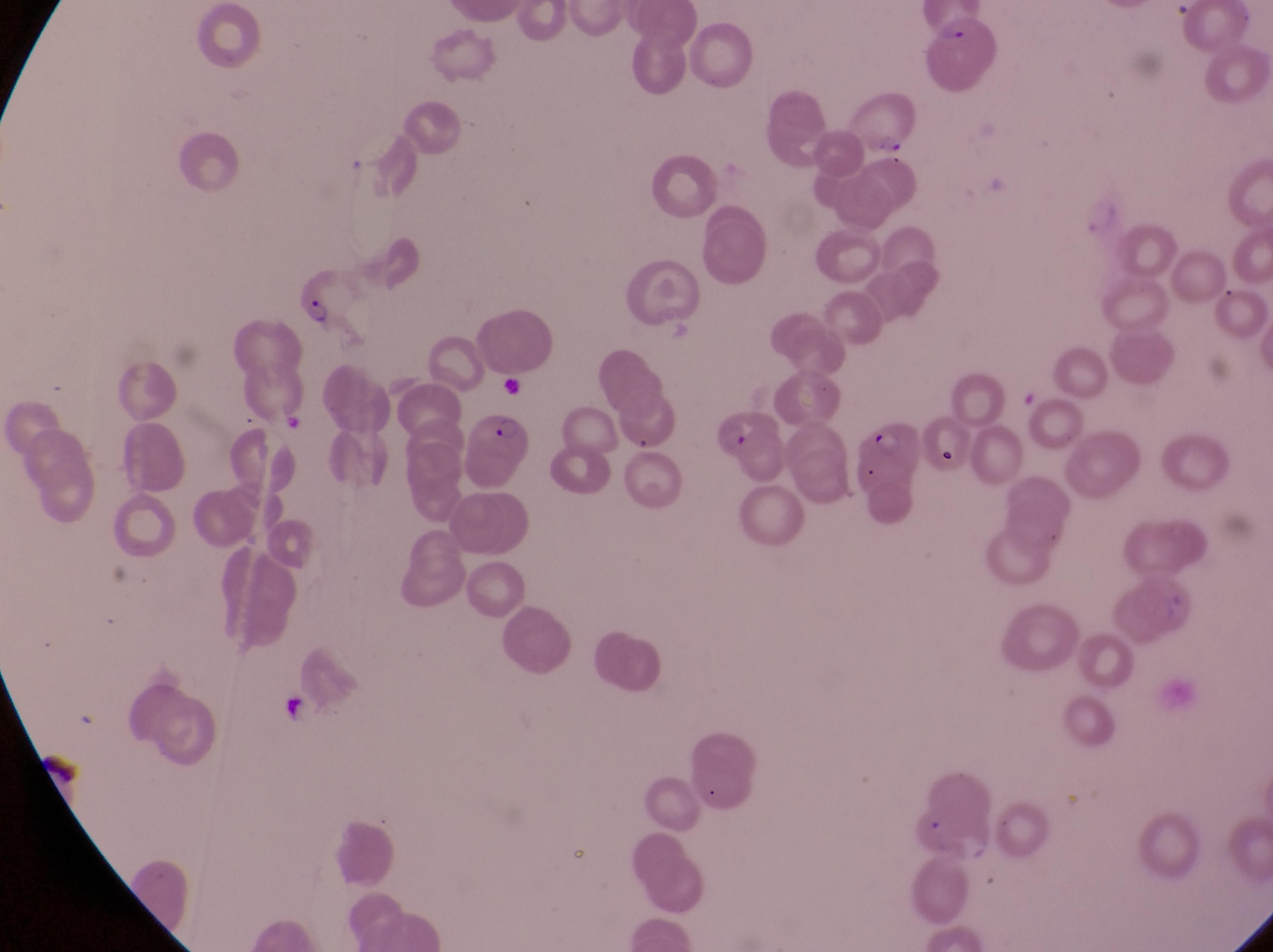
artifact_platelet_like_body_stain_precipitate_or_debris_locations: 'approximate bounding boxes as (left, top, right, bottom) in pixels: (274, 691, 326, 738)'
field_of_view: single
parasitised_red_blood_cell_locations: 'approximate bounding boxes as (left, top, right, bottom) in pixels: (928, 10, 1000, 87), (851, 85, 920, 153), (289, 260, 359, 328), (716, 404, 790, 482), (467, 410, 534, 477), (847, 417, 924, 482)'
preparation: thin blood film
country: Uganda
capture: smartphone photograph through the eyepiece of an Olympus CX-23 microscope
image_size: 1273×952 pixels
magnification: 1000x